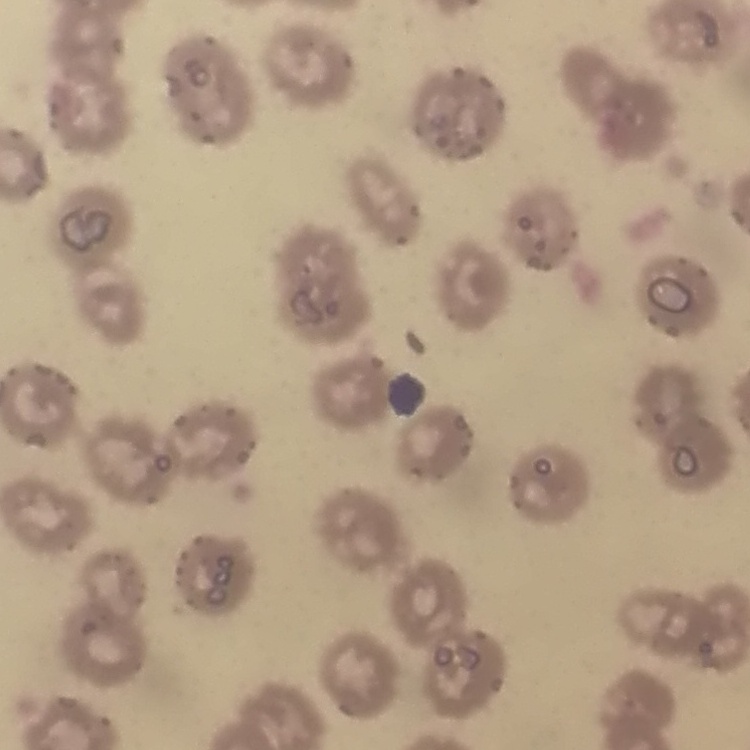

erythrocyte morphology = no rouleaux formation
stain = Field's or Giemsa
image type = one tile cut from a larger photomicrograph
preparation = thin blood film